Report the malaria status of this cell.
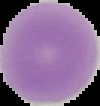
It is uninfected.

From a thin blood smear. Segmented cell region on a black background. Image is 100×106 pixels.